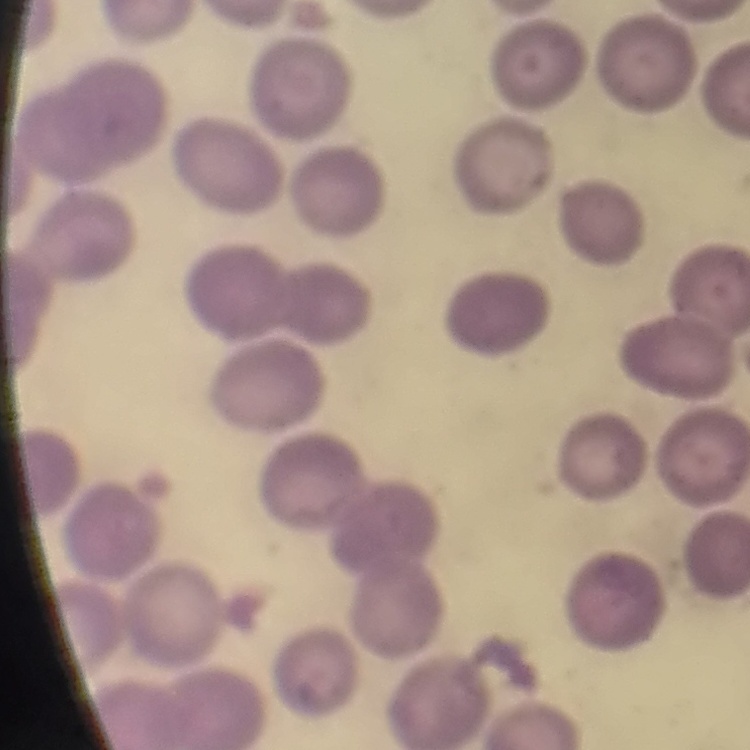

Summary:
  - Erythrocyte morphology: no rouleaux formation
  - Image type: square crop of a larger photomicrograph
  - Preparation: thin peripheral smear
  - Stain: Field's or Giemsa